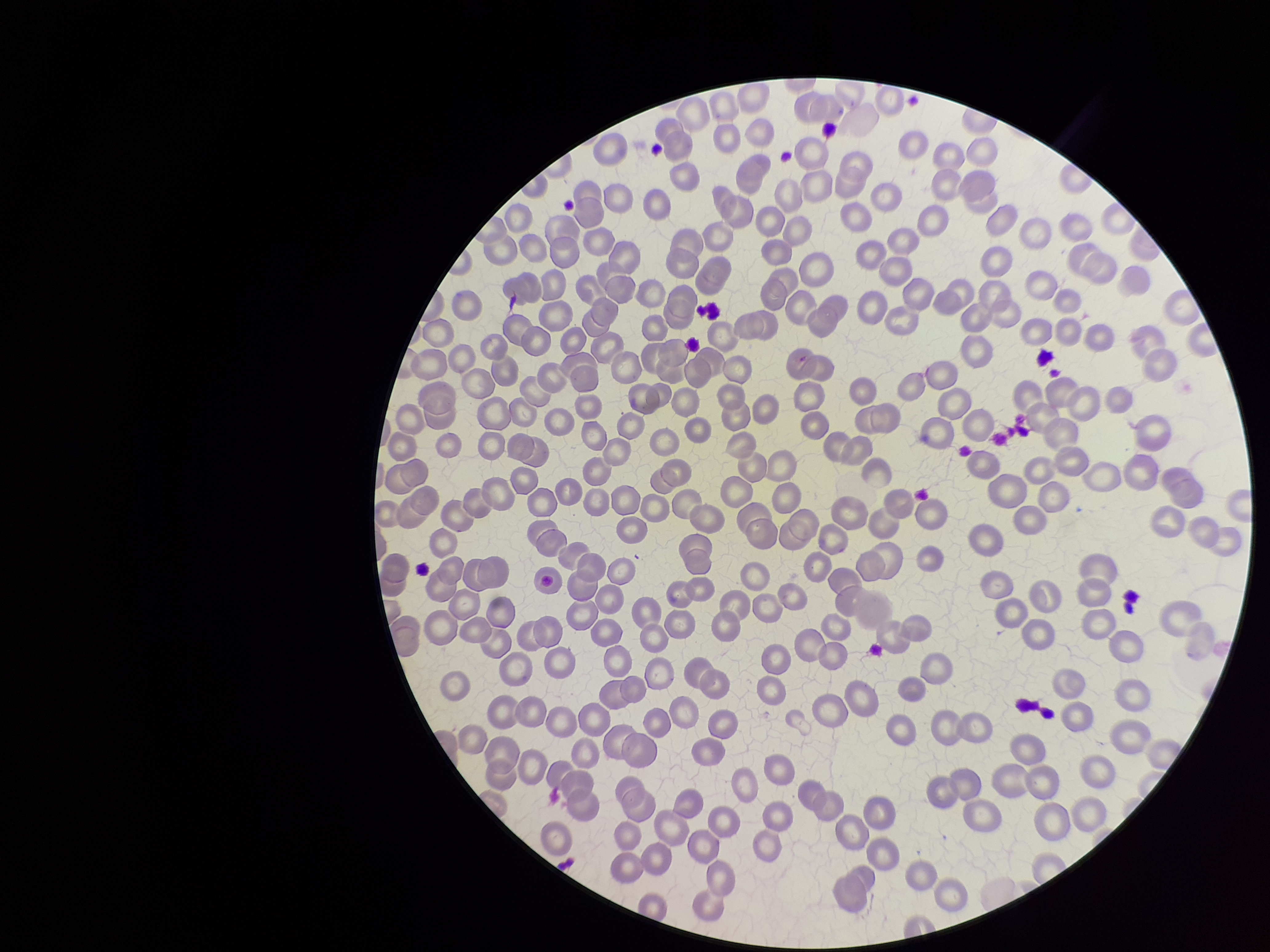
field_of_view: one from this slide
preparation: thin smear
capture: smartphone photograph through the microscope eyepiece
patient_malaria_status: negative
parasitized_red_blood_cells: none detected
stain: Giemsa
parasitized_red_blood_cell_count: 0
red_blood_cell_count: 239
image_size: 1270×952 pixels